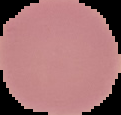
image_size: 121×115 pixels
preparation: thin blood film
image_type: segmented cell region on a black background
result: no Plasmodium parasites detected